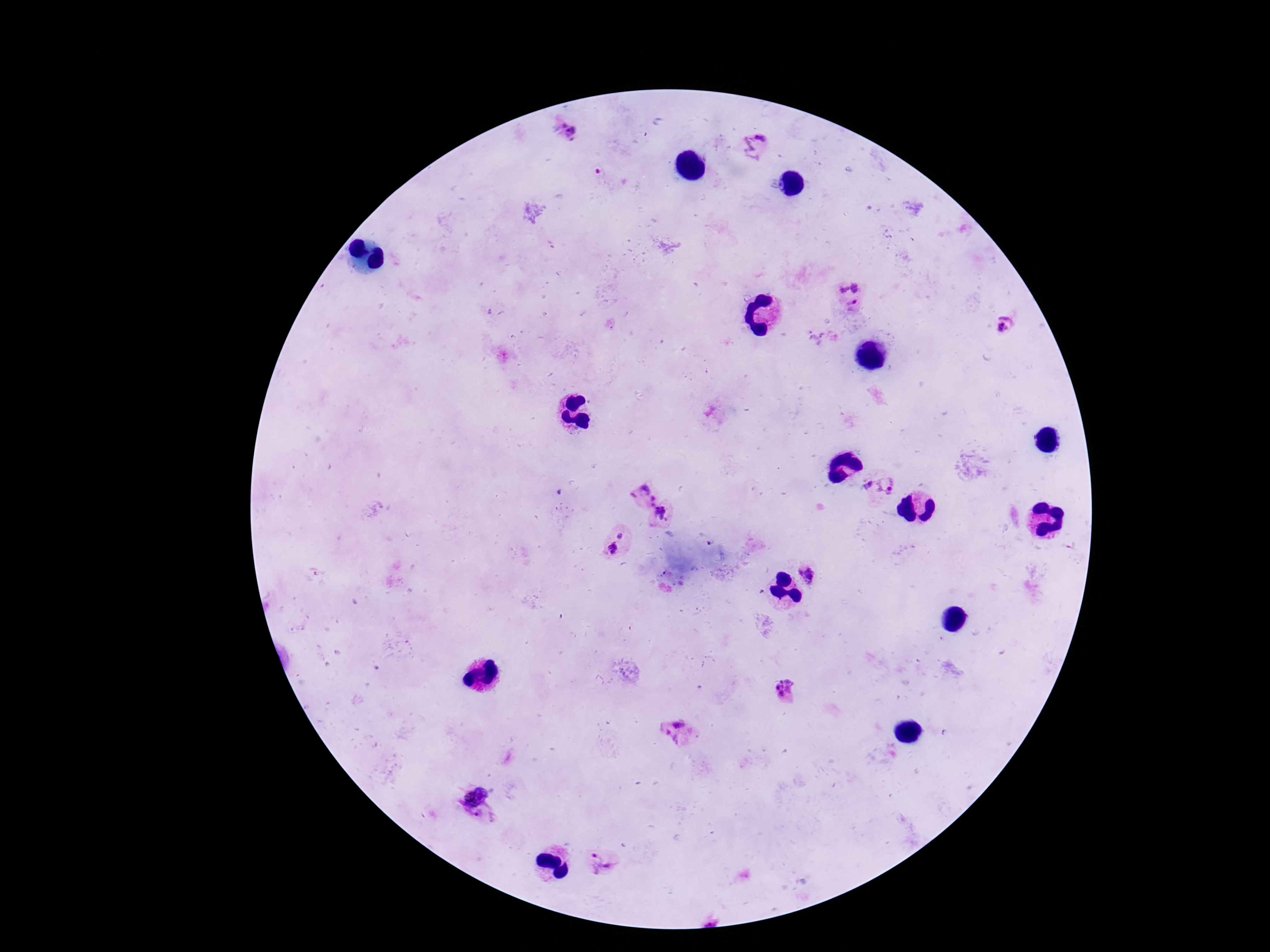

Approximate centers as {x, y} in pixels.
Summary:
  - Plasmodium parasite locations: {570, 131}, {756, 146}, {857, 285}, {844, 289}, {854, 304}, {1005, 325}, {868, 484}, {889, 484}, {644, 495}, {662, 515}, {621, 536}, {613, 548}, {809, 572}, {786, 690}, {679, 722}, {670, 739}, {471, 788}, {480, 815}, {603, 864}
  - Patient malaria status: positive
  - Stain: Giemsa
  - Image size: 1270×952 pixels
  - Preparation: thick blood smear
  - Field of view: single
  - Capture: smartphone camera through the microscope eyepiece
  - Magnification: 100x